Classify this cell by malaria status.
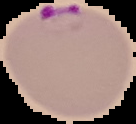
It is parasitized.

Image is 136×124 pixels. Segmented cell region on a black background. From a thin blood smear.